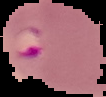 Result: malaria parasites identified. From a thin blood smear. Segmented cell region on a black background. Image is 106×97 pixels.